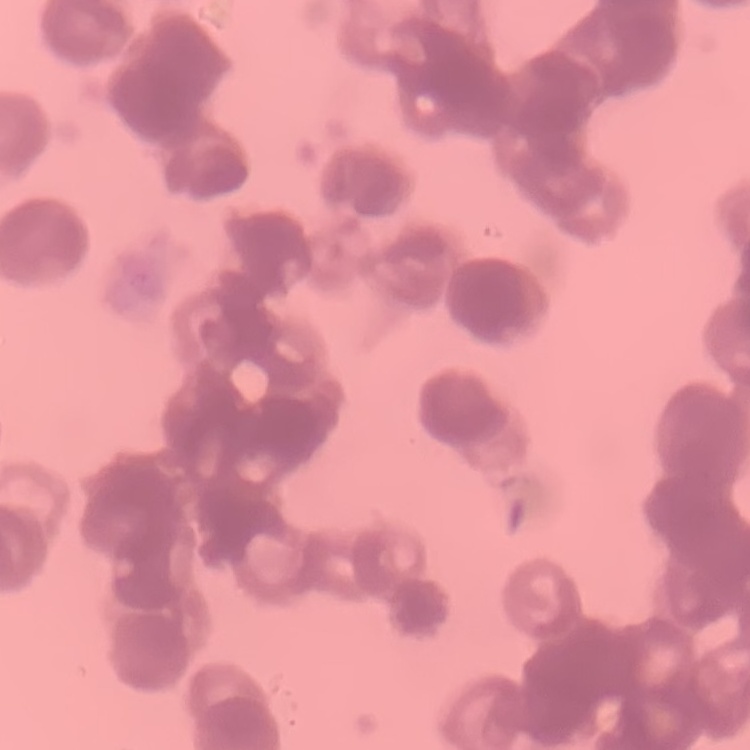
Summary:
  - Red blood cell morphology: rouleaux formation
  - Image type: square crop of a larger photomicrograph
  - Stain: Field's or Giemsa
  - Preparation: thin peripheral smear